Give the extent of all Plasmodium falciparum-infected red blood cells.
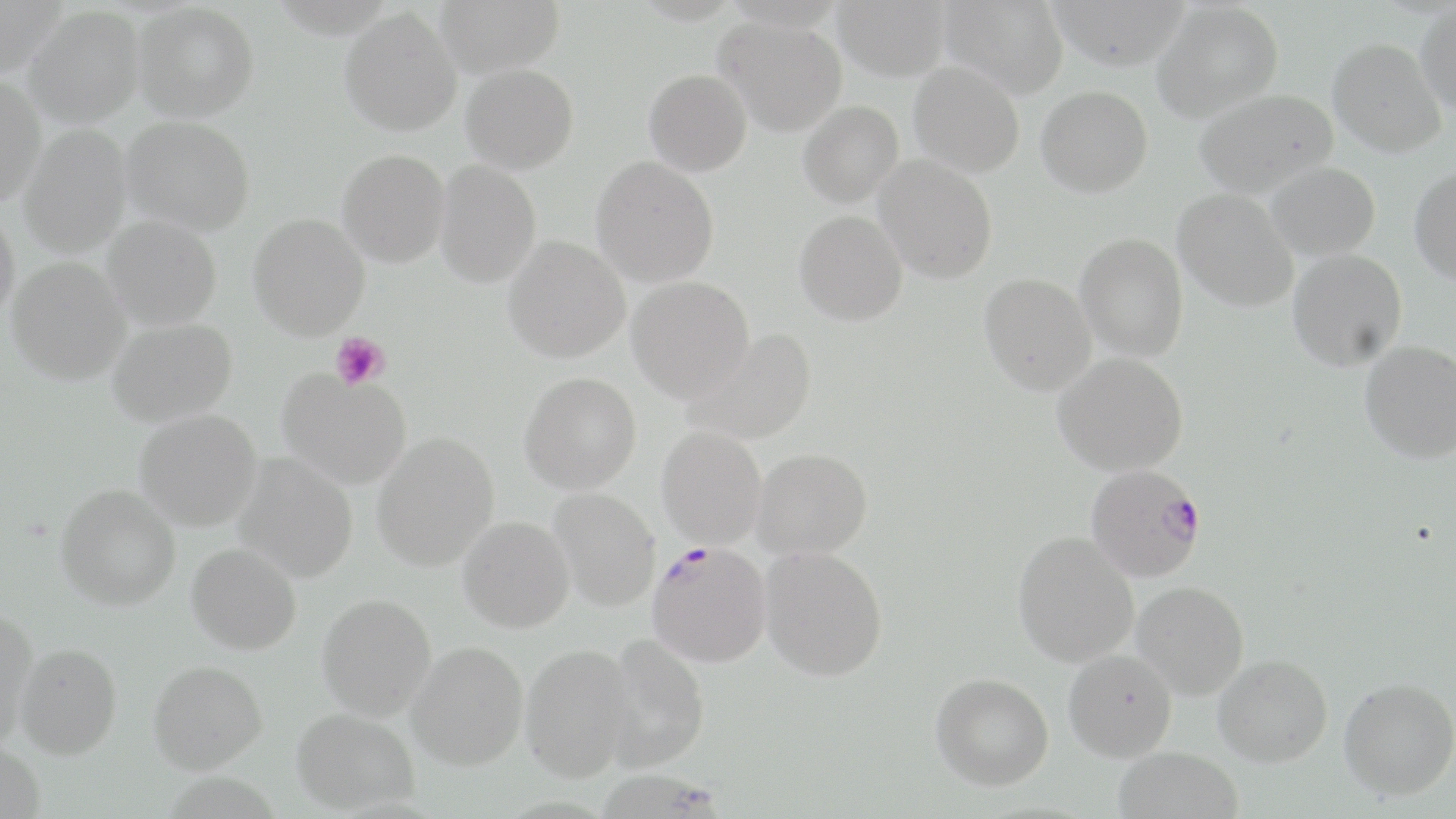
Approximate bounding boxes as (x1, y1, x2, y2) in pixels.
Plasmodium falciparum-infected red blood cells: (1085, 463, 1207, 582), (646, 540, 773, 667).

Summary:
  - Uninfected red blood cell locations: (0, 0, 67, 80), (434, 0, 566, 77), (833, 0, 951, 81), (938, 0, 1068, 99), (1047, 0, 1190, 71), (1152, 2, 1283, 122), (132, 3, 259, 122), (1415, 4, 1456, 115), (339, 7, 462, 136), (24, 8, 145, 128), (715, 18, 847, 137), (1329, 37, 1446, 157), (909, 62, 1024, 176), (461, 64, 579, 174), (643, 69, 752, 177), (0, 76, 47, 206), (1036, 85, 1153, 197), (1194, 89, 1337, 197), (798, 101, 904, 207), (121, 116, 254, 236), (19, 126, 132, 258), (337, 149, 450, 268), (874, 155, 998, 283), (591, 156, 719, 287), (435, 160, 541, 288), (1264, 162, 1380, 261), (1409, 167, 1456, 284), (1173, 189, 1299, 312), (0, 203, 20, 328), (794, 210, 908, 326), (248, 213, 370, 340), (102, 216, 222, 331), (1075, 233, 1188, 361), (502, 236, 631, 363), (1288, 249, 1407, 371), (6, 257, 130, 385), (979, 273, 1097, 394), (627, 277, 755, 403), (106, 317, 238, 427), (684, 329, 817, 446), (1360, 340, 1456, 463), (1053, 353, 1188, 476), (277, 370, 411, 490), (519, 372, 642, 494), (134, 409, 262, 531), (656, 426, 767, 549), (371, 433, 499, 571), (752, 448, 873, 560), (234, 453, 358, 583), (55, 484, 181, 610), (546, 488, 660, 612), (458, 516, 574, 633), (1013, 531, 1139, 667), (186, 543, 302, 655), (760, 546, 887, 681), (1132, 581, 1249, 699), (317, 594, 436, 721), (0, 609, 40, 751), (601, 634, 711, 773), (408, 642, 529, 771), (14, 643, 122, 759), (520, 644, 637, 782), (1063, 649, 1178, 762), (1213, 654, 1333, 767), (147, 660, 268, 774), (931, 672, 1054, 790), (1339, 677, 1456, 799), (292, 708, 420, 814), (0, 740, 46, 819), (1113, 747, 1243, 819)
  - Platelet locations: (330, 332, 390, 389)
  - Slide-level diagnosis: Plasmodium falciparum
  - Field of view: single
  - Image size: 1456×819 pixels
  - Magnification: 1000x
  - Preparation: thin blood film
  - Stain: May-Grünwald-Giemsa
  - Modality: optical microscopy